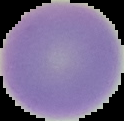

{
  "image_size": "124×121 pixels",
  "preparation": "thin blood film",
  "image_type": "segmented cell region with the area outside set to black",
  "malaria_status": "uninfected"
}